Report the malaria status of this cell.
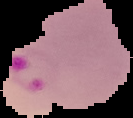
Parasitized.

{
  "image_size": "133×118 pixels",
  "image_type": "segmented cell region on a black background",
  "preparation": "thin blood smear"
}